Name the parasite shown.
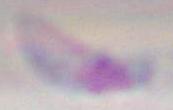
Toxoplasma gondii.

magnification = 1000x
modality = micrograph